Report the malaria status of this cell.
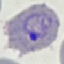

Parasitized.

Automatically extracted cell patch, resized to 64 × 64 pixels. Acquired by smartphone through the microscope eyepiece. Thin blood film. Giemsa stain.